Name the parasite shown.
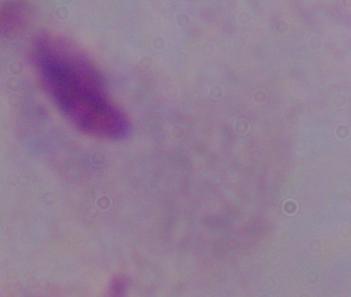

A trichomonad.

1000x magnification. Micrograph.